Locate platelets.
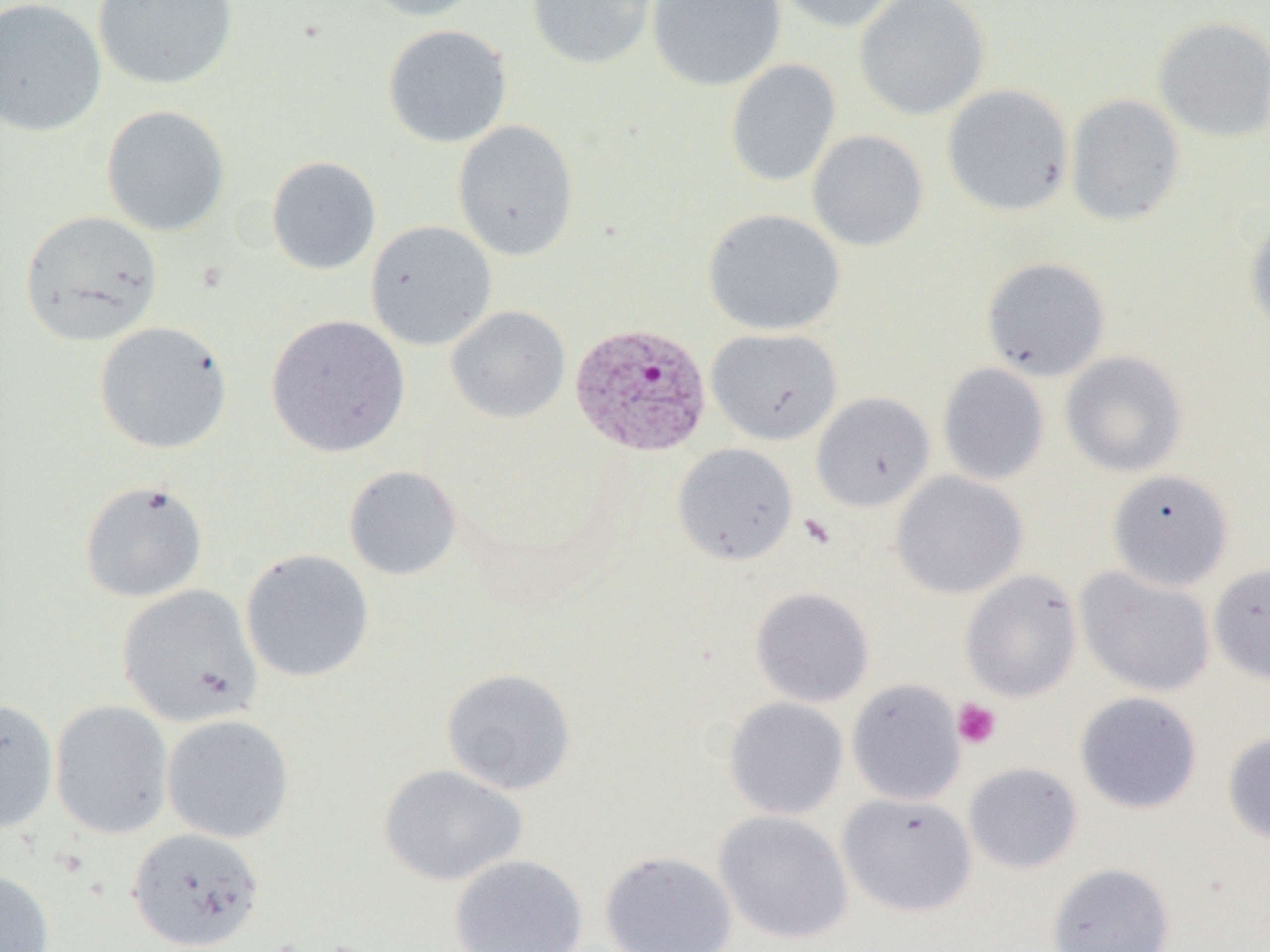
Approximate bounding boxes as [x1, y1, x2, y2] in pixels.
Platelets: [952, 699, 1001, 749].

Plasmodium vivax-infected red blood cell locations: [570, 322, 712, 458]. Uninfected red blood cell locations: [0, 0, 107, 138], [93, 0, 238, 90], [360, 0, 487, 21], [526, 0, 658, 70], [646, 0, 785, 91], [771, 0, 906, 33], [854, 0, 990, 121], [1153, 16, 1270, 142], [382, 24, 512, 148], [725, 58, 841, 188], [941, 84, 1074, 217], [1065, 94, 1185, 226], [100, 105, 230, 236], [453, 120, 579, 262], [806, 130, 929, 252], [267, 156, 381, 275], [702, 208, 846, 336], [20, 210, 163, 347], [1245, 216, 1270, 336], [365, 220, 498, 351], [981, 257, 1111, 381], [445, 306, 570, 423], [265, 314, 410, 457], [94, 321, 233, 454], [706, 328, 842, 445], [1059, 351, 1188, 477], [937, 362, 1050, 486], [811, 392, 935, 511], [672, 443, 798, 565], [343, 465, 463, 581], [1106, 468, 1234, 592], [890, 471, 1028, 599], [79, 480, 208, 603], [240, 549, 374, 682], [1208, 563, 1270, 686], [1075, 566, 1216, 698], [960, 569, 1082, 702], [117, 584, 263, 728], [750, 587, 874, 708], [441, 668, 576, 796], [846, 678, 966, 806], [1074, 691, 1203, 814], [0, 697, 59, 834], [723, 697, 849, 820], [49, 699, 174, 840], [161, 713, 295, 843], [1222, 731, 1270, 844], [963, 762, 1083, 874], [378, 764, 528, 887], [837, 792, 978, 918], [713, 809, 854, 945], [126, 826, 265, 950], [599, 849, 738, 952], [449, 853, 588, 952], [1047, 862, 1175, 952], [0, 869, 54, 952]. Slide-level diagnosis: Plasmodium vivax. Thin blood smear. Single field of view. Optical microscopy. Image is 1270×952 pixels. Captured at 1000x magnification.